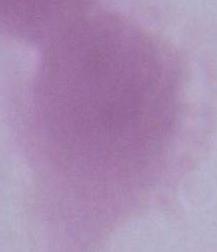

modality = photomicrograph
magnification = 1000x
identification = erythrocyte